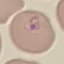
malaria_status: parasitized
capture: smartphone camera at the microscope eyepiece
stain: Giemsa
image_type: automatically extracted cell patch, resized to 64 × 64 pixels
preparation: thin blood smear